Report the malaria status of this cell.
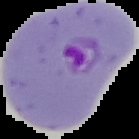
Parasitized.

Summary:
  - Image type: cell region segmented out of the field of view; surrounding area masked to black
  - Preparation: thin blood film
  - Image size: 139×139 pixels